Report the malaria status of this cell.
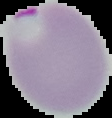
Parasitized.

preparation = thin blood smear
image type = segmented cell region with the area outside set to black
image size = 112×118 pixels